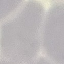 Malaria status: uninfected. Cell patch, automatically extracted from a larger field of view and resized to 64 × 64 pixels. Giemsa-stained preparation. Acquired by smartphone through the microscope eyepiece. Thin blood smear.